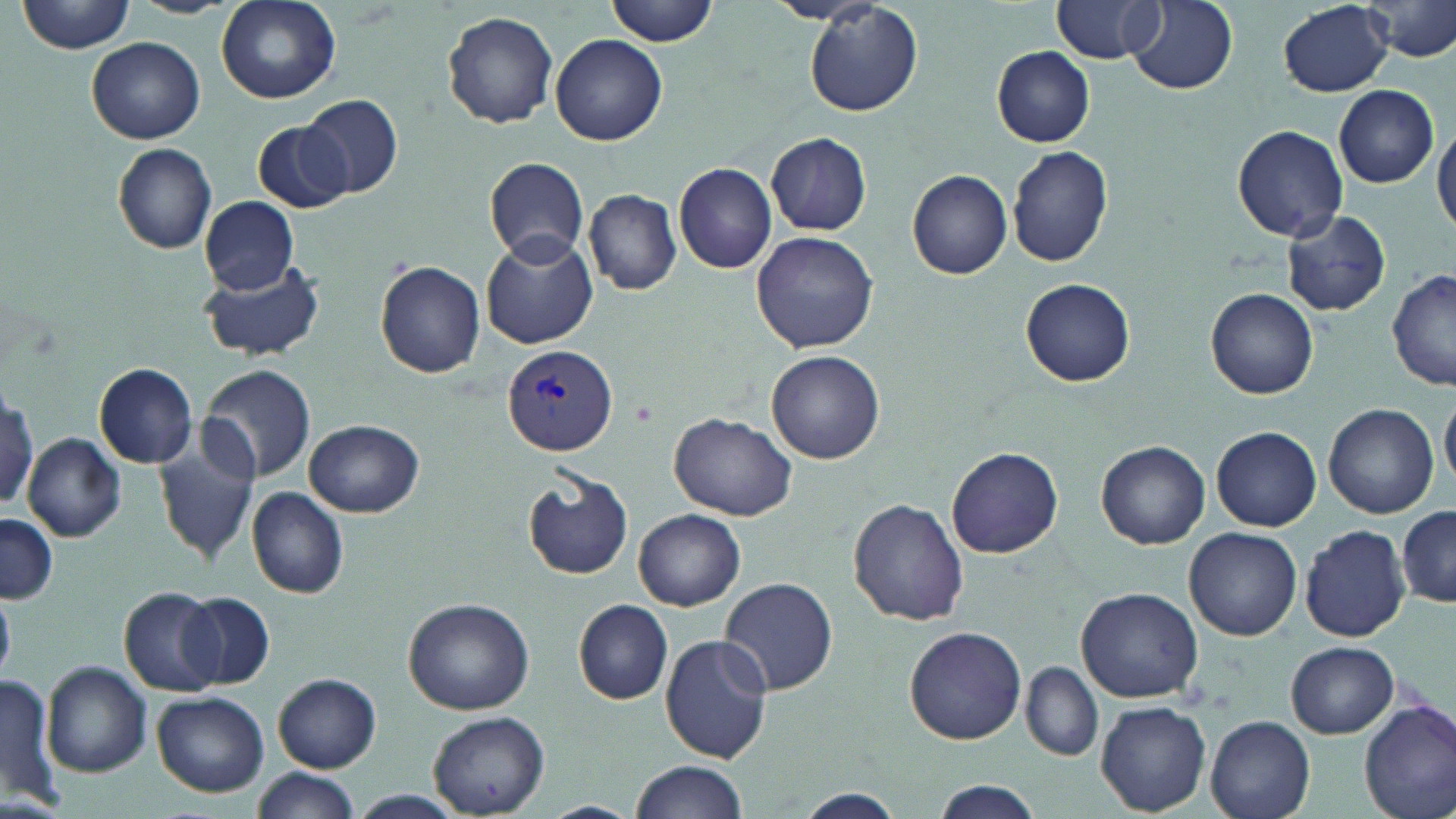
{
  "plasmodium_vivax_infected_red_blood_cell_locations": "approximate bounding boxes as (x1,y1)-(x2,y2) corner pairs in pixels: (501,345)-(620,455)",
  "slide_level_diagnosis": "Plasmodium vivax",
  "field_of_view": "single",
  "stain": "May-Grünwald-Giemsa",
  "preparation": "thin blood film",
  "magnification": "1000x",
  "uninfected_red_blood_cell_locations": "approximate bounding boxes as (x1,y1)-(x2,y2) corner pairs in pixels: (17,0)-(140,54), (606,0)-(721,46), (1053,0)-(1163,65), (1127,1)-(1238,93), (1278,1)-(1394,97), (1367,1)-(1456,62), (216,2)-(343,106), (804,2)-(921,116), (442,10)-(559,128), (552,34)-(667,146), (86,36)-(206,145), (993,46)-(1095,147), (1334,84)-(1438,187), (301,94)-(404,198), (251,120)-(349,214), (1432,121)-(1456,237), (1231,124)-(1349,243), (766,133)-(872,235), (113,143)-(217,254), (1006,144)-(1113,267), (484,157)-(590,264), (673,162)-(778,273), (906,170)-(1011,278), (583,187)-(680,294), (200,196)-(298,291), (1280,210)-(1392,316), (750,231)-(878,354), (479,233)-(596,349), (197,257)-(327,361), (376,260)-(485,378), (1387,270)-(1456,391), (1020,279)-(1136,386), (1206,287)-(1319,399), (766,349)-(885,463), (94,362)-(199,468), (198,362)-(317,483), (2,387)-(38,515), (1441,391)-(1456,488), (1323,402)-(1440,518), (670,413)-(799,520), (304,418)-(423,518), (1211,426)-(1321,531), (152,428)-(263,565), (22,433)-(126,542), (1097,440)-(1211,548), (947,446)-(1063,559), (522,472)-(634,581), (246,487)-(350,599), (848,497)-(968,625), (1397,506)-(1456,605), (633,509)-(746,611), (0,515)-(56,606), (1299,523)-(1412,642), (1185,527)-(1302,640), (718,576)-(838,696), (119,585)-(224,697), (1076,586)-(1204,701), (177,590)-(275,691), (403,597)-(534,714), (574,600)-(673,705), (904,626)-(1026,745), (659,634)-(774,763), (1286,640)-(1397,738), (41,662)-(151,776), (1021,663)-(1103,761), (274,673)-(380,772), (0,674)-(59,809), (153,691)-(269,797), (1359,699)-(1456,819), (1096,701)-(1212,817), (427,711)-(549,818), (1207,716)-(1315,819), (631,759)-(749,819), (251,767)-(361,818), (928,779)-(1045,819), (786,790)-(912,818)",
  "image_size": "1456×819 pixels",
  "modality": "optical microscopy"
}